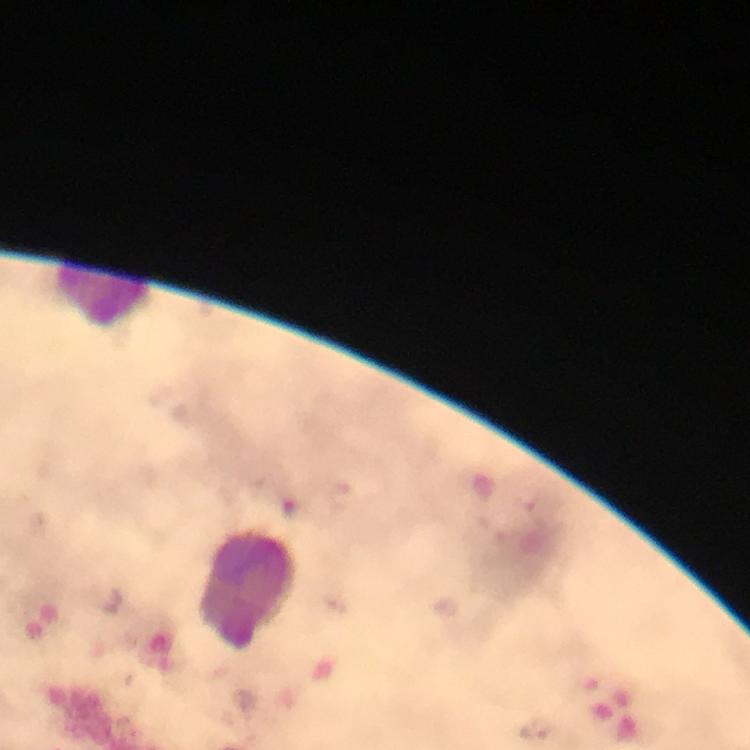
Approximate centers as {x, y} in pixels. Leukocyte locations: {104, 297}, {248, 589}. Malaria parasite locations: {539, 729}. Immersion oil was used. At 100x magnification. From a diagnostic examination for malaria. Smartphone photograph taken through a microscope. Image is 750×750 pixels. A crop from one field of view. Giemsa-stained preparation. Thick blood film.